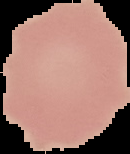

Summary:
  - Preparation: thin blood film
  - Image size: 130×154 pixels
  - Malaria status: uninfected
  - Image type: cell region segmented out of the field of view; surrounding area masked to black